Classify this cell by malaria status.
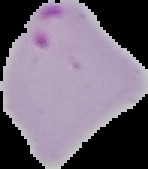
It is parasitized.

The area outside the segmented cell region is set to black. Image is 148×169 pixels. From a thin blood film.